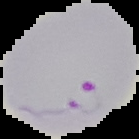
Summary:
  - Image size: 139×139 pixels
  - Result: Plasmodium parasites detected
  - Preparation: thin blood film
  - Image type: segmented cell region on a black background